Locate every malaria parasite and every leukocyte.
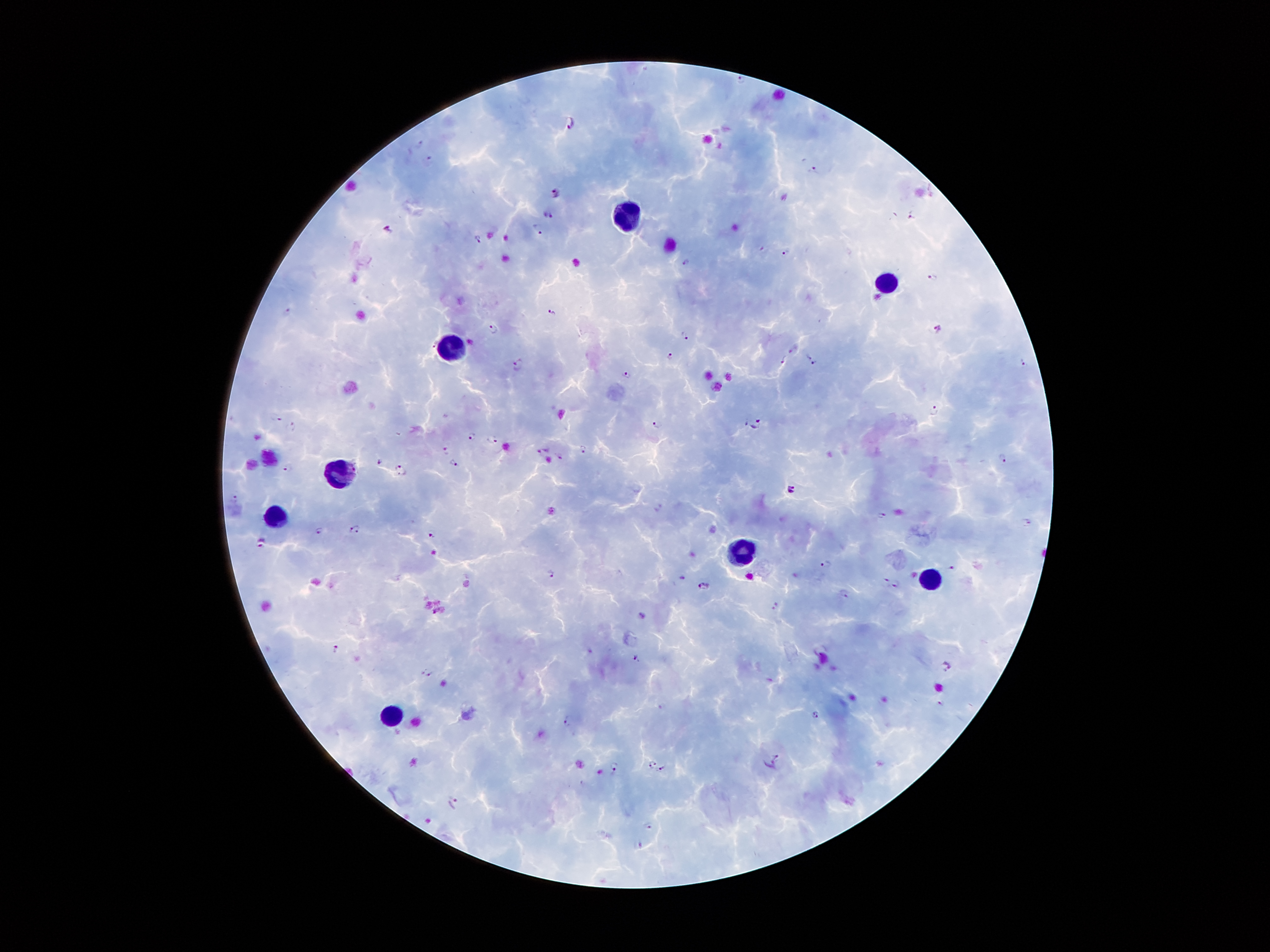

Approximate centers as [x, y] in pixels.
Malaria parasites: [568, 122], [419, 143], [430, 160], [813, 168], [556, 192], [548, 213], [913, 215], [537, 228], [389, 230], [478, 238], [788, 252], [685, 263], [932, 275], [551, 311], [286, 314], [494, 329], [939, 330], [685, 335], [434, 343], [793, 349], [808, 355], [671, 358], [785, 360], [1023, 360], [816, 363], [519, 364], [628, 374], [933, 410], [275, 417], [657, 423], [757, 425], [291, 428], [471, 436], [492, 439], [582, 449], [542, 450], [446, 451], [559, 456], [1004, 459], [380, 462], [454, 462], [288, 466], [402, 469], [790, 489], [234, 498], [656, 507], [882, 515], [1028, 521], [353, 529], [322, 530], [432, 534], [261, 543], [827, 564], [950, 566], [550, 573], [884, 581], [896, 582], [704, 586], [843, 593], [778, 606], [644, 617], [336, 648], [637, 658], [946, 665], [428, 672], [939, 703], [816, 714], [569, 721], [777, 757], [653, 765], [615, 767], [662, 769], [452, 803], [649, 825], [638, 844].
Leukocytes: [630, 217], [890, 285], [453, 348], [343, 474], [279, 517], [741, 555], [931, 578], [396, 717].

Summary:
  - Capture: smartphone through the microscope eyepiece
  - Image size: 1270×952 pixels
  - Patient malaria status: infected with Plasmodium falciparum
  - Stain: Giemsa
  - Field of view: single
  - Preparation: thick blood film
  - Magnification: 100x